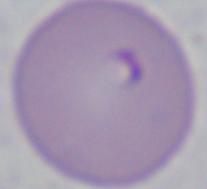

Summary:
  - Modality: micrograph
  - Identification: Babesia
  - Magnification: 1000x